Locate and identify every blood parasite.
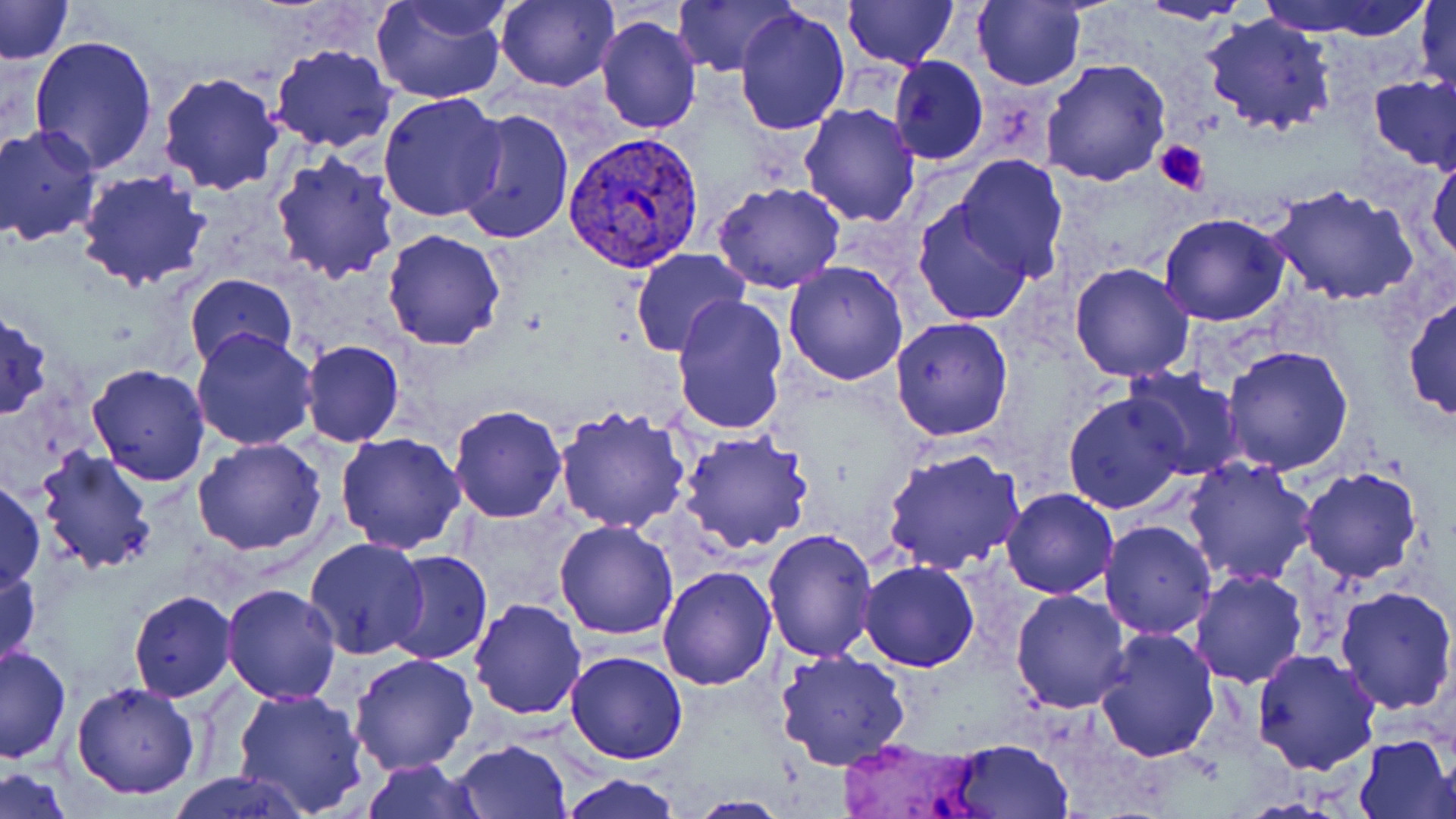

Approximate bounding boxes as (x1, y1, x2, y2) in pixels.
Plasmodium vivax-infected red blood cells: (565, 131, 704, 272).
No Plasmodium falciparum, Plasmodium ovale, Plasmodium malariae, Babesia divergens, or Trypanosoma brucei observed.

Platelet locations: (1154, 140, 1208, 195). Uninfected red blood cell locations: (0, 0, 74, 65), (371, 0, 510, 106), (495, 0, 619, 92), (671, 0, 796, 77), (843, 0, 959, 70), (1257, 0, 1432, 40), (1414, 0, 1455, 102), (973, 1, 1085, 90), (1137, 1, 1255, 27), (734, 7, 851, 136), (1199, 12, 1337, 137), (594, 14, 702, 135), (29, 34, 161, 176), (268, 44, 397, 152), (887, 55, 987, 165), (1042, 59, 1173, 187), (157, 71, 284, 195), (1369, 77, 1456, 170), (377, 92, 509, 223), (799, 102, 922, 226), (455, 107, 577, 249), (1, 126, 103, 246), (1426, 147, 1456, 266), (270, 150, 403, 285), (955, 155, 1068, 279), (75, 172, 212, 292), (712, 182, 845, 294), (1268, 185, 1419, 306), (912, 198, 1035, 326), (1158, 212, 1289, 327), (382, 229, 507, 350), (628, 249, 750, 359), (783, 261, 910, 386), (1068, 263, 1195, 383), (184, 273, 297, 368), (670, 293, 790, 437), (1403, 294, 1456, 421), (0, 307, 52, 421), (891, 318, 1013, 441), (192, 328, 318, 451), (300, 340, 404, 448), (1221, 347, 1354, 474), (87, 363, 210, 486), (1121, 365, 1243, 479), (1062, 391, 1190, 515), (448, 404, 568, 523), (553, 404, 694, 536), (678, 430, 814, 554), (335, 432, 467, 553), (193, 438, 328, 555), (33, 444, 159, 575), (881, 447, 1027, 576), (1184, 456, 1318, 586), (1297, 467, 1424, 584), (0, 476, 44, 594), (1001, 488, 1118, 599), (553, 519, 680, 639), (1099, 520, 1217, 639), (762, 528, 879, 663), (303, 538, 429, 659), (382, 549, 494, 666), (859, 561, 979, 671), (0, 562, 41, 675), (658, 566, 776, 690), (1189, 568, 1308, 687), (222, 582, 343, 703), (1334, 586, 1456, 714), (127, 589, 237, 702), (1010, 589, 1131, 713), (468, 599, 586, 720), (1093, 626, 1220, 763), (1, 645, 72, 763), (1251, 647, 1381, 774), (774, 649, 913, 771), (566, 650, 689, 764), (349, 653, 477, 774), (71, 681, 200, 800), (232, 685, 370, 816), (1353, 733, 1453, 817), (451, 739, 573, 819), (947, 740, 1072, 817), (1432, 750, 1456, 816), (361, 759, 485, 819), (0, 768, 72, 818), (168, 770, 310, 818), (558, 774, 683, 818), (685, 796, 793, 818). Slide-level diagnosis: Plasmodium vivax. Light microscopy. Captured at 1000x magnification. Image is 1456×819 pixels. One field of a larger specimen. Thin blood smear. May-Grünwald-Giemsa-stained preparation.